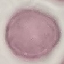

malaria_status: uninfected
preparation: thin blood smear
capture: smartphone camera at the microscope eyepiece
image_type: automatically extracted cell patch, resized to 64 × 64 pixels
stain: Giemsa